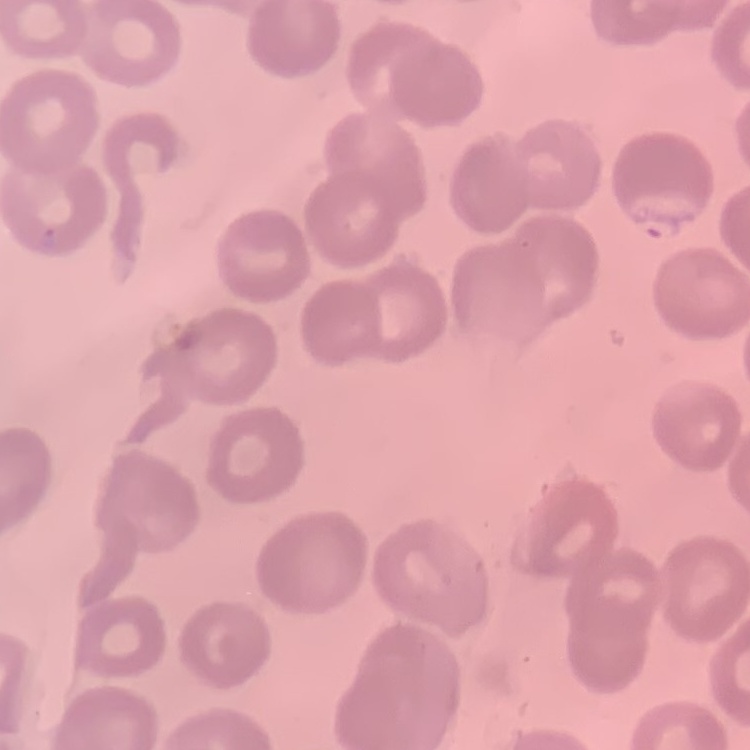

erythrocyte_morphology: no rouleaux formation
image_type: square crop of a larger photomicrograph
stain: Field's or Giemsa
preparation: thin blood film